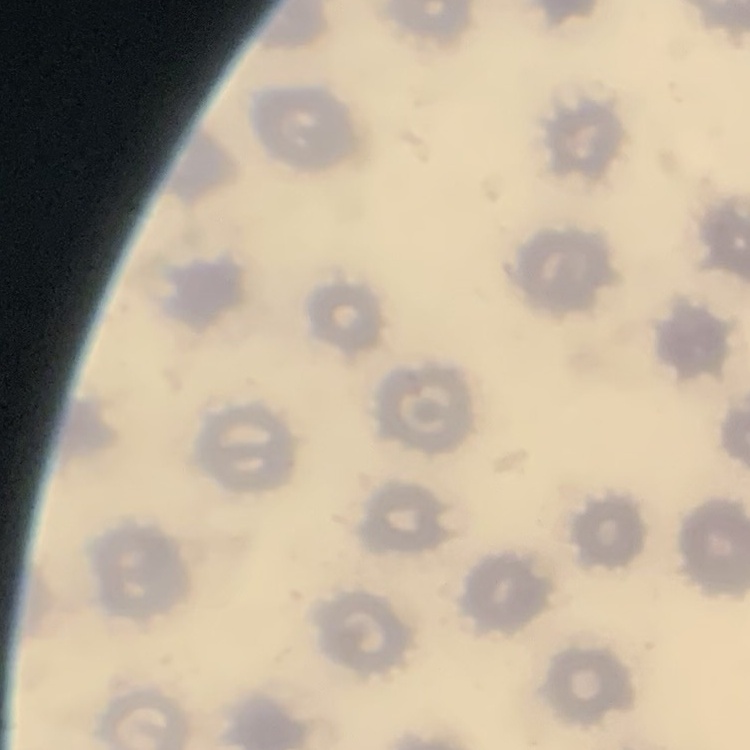
Summary:
  - Red blood cell morphology: no rouleaux formation
  - Image type: one tile cut from a larger photomicrograph
  - Stain: Field's or Giemsa
  - Preparation: thin blood smear